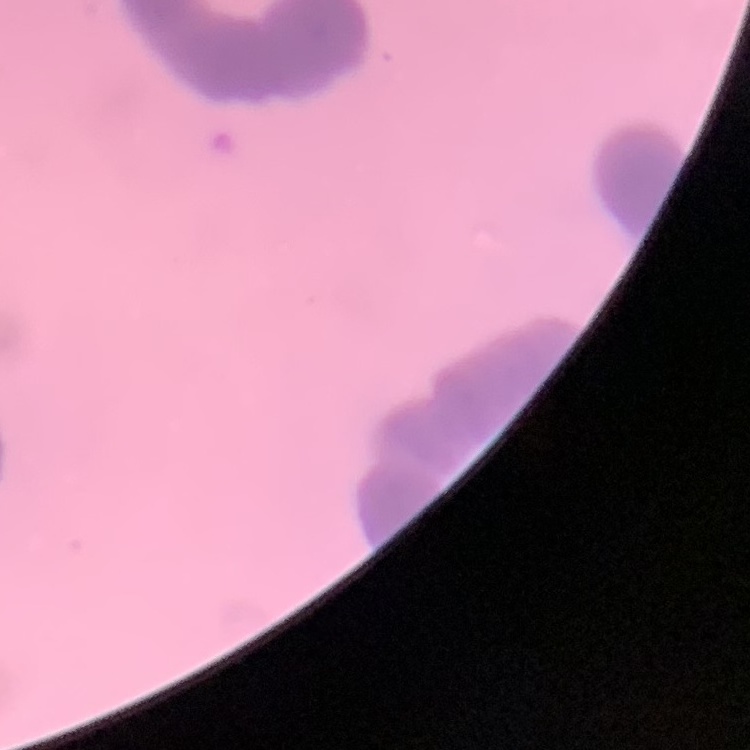

erythrocyte morphology = rouleaux formation
stain = Field's or Giemsa
image type = one tile cut from a larger photomicrograph
preparation = thin blood film